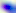

Summary:
  - Identification: Toxoplasma gondii
  - Magnification: 400x
  - Modality: photomicrograph